Classify this cell by malaria status.
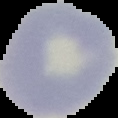
It is uninfected.

From a thin blood smear. The area outside the segmented cell region is set to black. Image is 118×118 pixels.